Locate and identify every blood parasite.
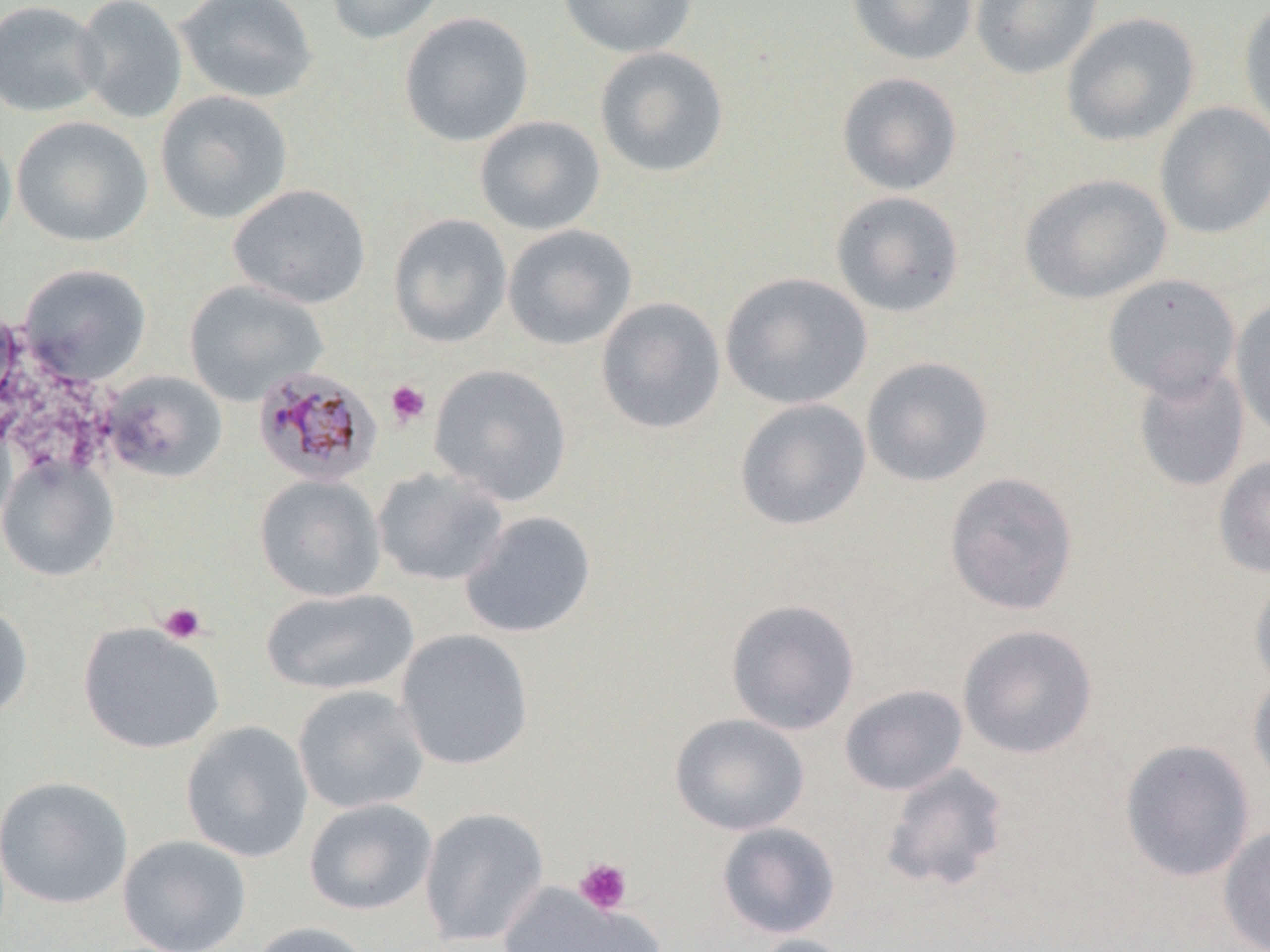

Approximate bounding boxes as (x1, y1, x2, y2) in pixels.
Plasmodium malariae-infected red blood cells: (252, 366, 382, 488).
No Plasmodium falciparum, Plasmodium ovale, Plasmodium vivax, Babesia divergens, or Trypanosoma brucei observed.

slide-level diagnosis = Plasmodium malariae
magnification = 1000x
preparation = thin blood smear
image size = 1270×952 pixels
uninfected red blood cell locations = approximate bounding boxes as (x1, y1, x2, y2) in pixels: (0, 0, 106, 117), (72, 0, 188, 124), (174, 0, 318, 105), (323, 0, 447, 45), (557, 0, 698, 59), (847, 0, 978, 66), (970, 0, 1103, 80), (1238, 2, 1270, 137), (399, 12, 534, 148), (1061, 12, 1200, 147), (594, 46, 730, 179), (837, 72, 962, 196), (154, 90, 293, 224), (1154, 102, 1270, 240), (11, 115, 153, 248), (474, 115, 606, 235), (0, 123, 17, 254), (1019, 172, 1172, 304), (228, 183, 371, 309), (830, 190, 965, 318), (388, 213, 512, 348), (502, 224, 637, 350), (18, 263, 151, 385), (719, 272, 873, 410), (1102, 273, 1241, 401), (183, 279, 329, 406), (595, 296, 726, 436), (1230, 297, 1270, 439), (860, 356, 994, 487), (429, 363, 572, 506), (1133, 363, 1250, 493), (99, 370, 228, 483), (734, 398, 871, 532), (0, 455, 119, 582), (1213, 455, 1270, 578), (372, 467, 509, 587), (943, 471, 1080, 616), (254, 473, 385, 602), (460, 510, 596, 638), (1249, 573, 1270, 694), (260, 587, 419, 697), (725, 598, 861, 735), (0, 602, 33, 722), (78, 622, 224, 754), (957, 624, 1098, 760), (395, 628, 534, 771), (1248, 674, 1270, 793), (838, 684, 969, 797), (292, 685, 429, 815), (669, 713, 809, 836), (180, 720, 314, 863), (1118, 738, 1256, 883), (878, 762, 1012, 893), (0, 775, 134, 909), (303, 797, 438, 916), (418, 806, 549, 948), (716, 822, 841, 939), (1217, 823, 1270, 952), (117, 834, 252, 952), (498, 883, 661, 952), (247, 921, 376, 952), (746, 934, 860, 952)
stain = May-Grünwald-Giemsa
field of view = single
modality = optical microscopy
platelet locations = approximate bounding boxes as (x1, y1, x2, y2) in pixels: (385, 380, 430, 427), (158, 602, 207, 644), (574, 858, 632, 915)